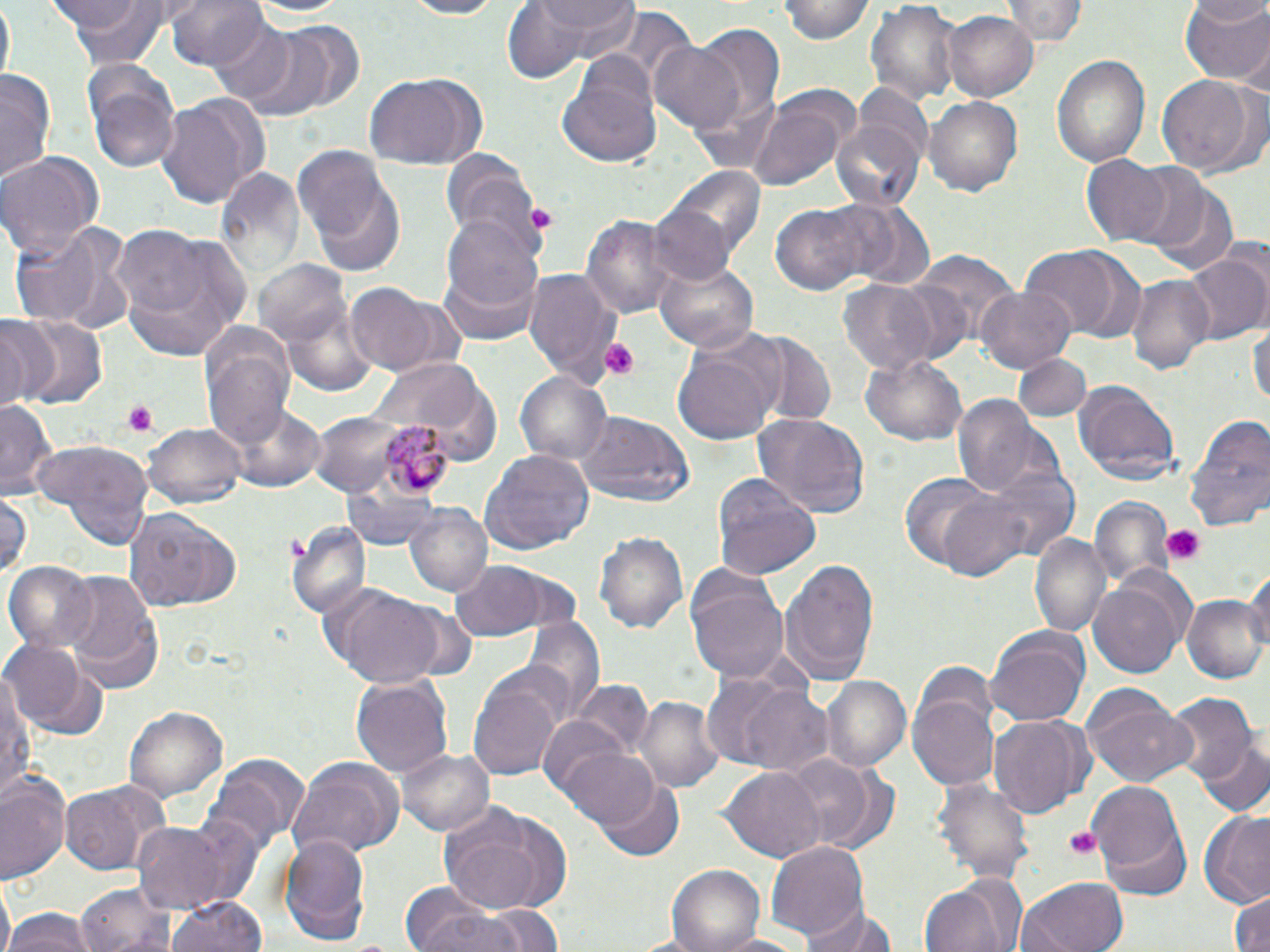

slide-level diagnosis = Plasmodium malariae
preparation = thin blood film
platelet locations = approximate bounding boxes as [x1, y1, x2, y2] in pixels: [601, 340, 638, 381], [121, 401, 160, 435], [1160, 525, 1209, 567], [1061, 825, 1104, 861]
field of view = single
modality = light microscopy
Plasmodium malariae-infected red blood cell locations = approximate bounding boxes as [x1, y1, x2, y2] in pixels: [382, 423, 456, 496]
magnification = 1000x
image size = 1270×952 pixels
uninfected red blood cell locations = approximate bounding boxes as [x1, y1, x2, y2] in pixels: [53, 0, 175, 65], [167, 0, 268, 72], [238, 0, 356, 22], [396, 0, 506, 19], [539, 0, 638, 53], [780, 0, 873, 44], [866, 0, 961, 105], [1007, 0, 1089, 46], [1181, 0, 1270, 85], [498, 1, 592, 82], [1, 3, 13, 86], [601, 6, 696, 100], [945, 11, 1036, 101], [201, 17, 297, 101], [235, 23, 358, 117], [693, 26, 786, 126], [647, 42, 747, 135], [1053, 54, 1150, 167], [558, 60, 663, 170], [1, 67, 56, 185], [88, 69, 181, 176], [361, 72, 483, 169], [1157, 76, 1257, 173], [850, 83, 932, 175], [746, 89, 858, 191], [154, 92, 261, 211], [925, 94, 1023, 198], [833, 116, 926, 213], [292, 144, 393, 249], [0, 151, 105, 261], [440, 151, 542, 255], [1081, 155, 1173, 244], [215, 166, 307, 288], [1124, 166, 1211, 253], [672, 168, 766, 263], [308, 181, 405, 275], [1155, 187, 1239, 276], [835, 199, 932, 287], [647, 201, 736, 287], [769, 203, 870, 298], [582, 212, 676, 322], [439, 213, 545, 337], [13, 220, 135, 334], [111, 223, 252, 364], [1019, 245, 1137, 339], [913, 251, 1019, 348], [1183, 255, 1268, 345], [654, 257, 760, 353], [255, 261, 354, 352], [523, 267, 618, 383], [1126, 273, 1214, 376], [834, 279, 947, 377], [343, 284, 449, 376], [975, 288, 1077, 373], [0, 315, 57, 409], [10, 316, 108, 411], [1249, 318, 1269, 412], [743, 332, 837, 424], [200, 335, 295, 453], [672, 342, 778, 445], [861, 349, 966, 446], [1012, 355, 1094, 421], [377, 357, 500, 463], [515, 371, 612, 467], [1074, 380, 1180, 484], [949, 394, 1049, 501], [225, 396, 328, 492], [0, 402, 57, 495], [306, 408, 425, 500], [574, 411, 694, 507], [1185, 412, 1267, 531], [754, 413, 869, 518], [142, 421, 247, 510], [36, 439, 152, 548], [481, 450, 594, 557], [987, 468, 1079, 562], [898, 471, 1004, 573], [712, 473, 820, 581], [933, 487, 1047, 585], [1, 489, 30, 585], [1089, 495, 1175, 591], [405, 504, 493, 597], [122, 509, 242, 614], [288, 521, 370, 619], [595, 530, 689, 637], [1029, 531, 1112, 640], [779, 557, 881, 685], [450, 562, 550, 640], [6, 563, 99, 655], [1244, 565, 1270, 664], [59, 574, 165, 692], [688, 575, 788, 685], [1088, 579, 1186, 682], [331, 585, 452, 688], [1183, 595, 1267, 682], [519, 613, 606, 722], [986, 626, 1091, 729], [4, 635, 98, 732], [467, 667, 563, 784], [1, 670, 32, 803], [350, 675, 453, 778], [821, 676, 910, 772], [572, 681, 653, 760], [739, 684, 834, 775], [909, 687, 1000, 793], [1083, 689, 1196, 788], [1167, 694, 1256, 786], [635, 695, 723, 793], [126, 707, 225, 801], [988, 715, 1090, 816], [535, 716, 629, 802], [1195, 738, 1270, 819], [398, 746, 494, 837], [560, 748, 662, 833], [203, 752, 308, 853], [780, 754, 883, 853], [287, 757, 405, 858], [722, 766, 824, 861], [0, 773, 70, 882], [934, 775, 1034, 884], [597, 779, 686, 862], [1088, 779, 1185, 876], [60, 783, 162, 875], [438, 800, 572, 917], [1199, 810, 1270, 904], [1098, 821, 1192, 901], [135, 822, 231, 914], [279, 834, 371, 944], [766, 839, 868, 942], [669, 864, 766, 952], [921, 872, 1024, 952], [1019, 877, 1128, 952], [77, 882, 177, 952], [404, 884, 505, 952], [1227, 890, 1269, 952], [167, 893, 267, 952], [805, 898, 896, 951], [478, 904, 567, 951], [6, 909, 95, 952], [710, 932, 812, 952]
stain = May-Grünwald-Giemsa